Locate every malaria parasite.
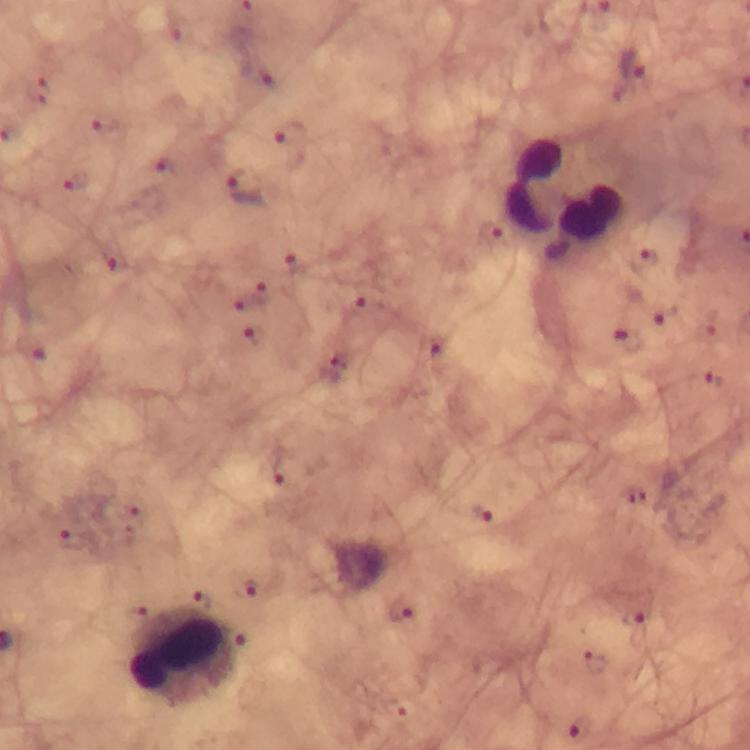
Approximate centers as {x, y} in pixels.
Malaria parasites: {632, 66}, {268, 78}, {40, 89}, {107, 125}, {166, 166}, {78, 181}, {245, 186}, {492, 234}, {650, 257}, {117, 259}, {362, 307}, {664, 312}, {254, 334}, {629, 338}, {433, 346}, {715, 381}, {277, 472}, {480, 511}, {75, 538}, {252, 587}, {402, 611}, {632, 619}, {583, 728}.

{
  "immersion_oil": "applied",
  "stain": "Giemsa",
  "preparation": "thick smear",
  "leukocyte_locations": "approximate centers as {x, y} in pixels: {568, 197}, {180, 657}",
  "magnification": "100x",
  "image_size": "750×750 pixels",
  "capture": "smartphone camera through the microscope",
  "cropped_from": "one field of view",
  "context": "from a diagnostic examination for malaria"
}